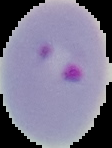

Summary:
  - Image type: segmented cell region with the area outside set to black
  - Preparation: thin blood smear
  - Result: malaria parasites detected
  - Image size: 112×148 pixels